Classify this cell by malaria status.
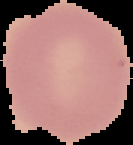
Uninfected.

Segmented cell region on a black background. From a thin blood smear. Image is 133×145 pixels.